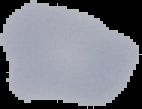

{
  "image_type": "cell region segmented out of the field of view; surrounding area masked to black",
  "preparation": "thin blood film",
  "image_size": "142×109 pixels",
  "malaria_status": "uninfected"
}